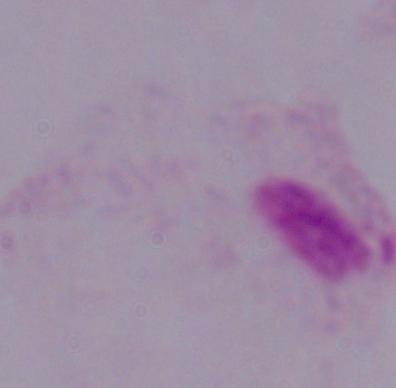

magnification: 1000x
identification: trichomonad
modality: micrograph